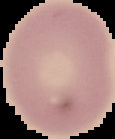

Summary:
  - Preparation: thin blood film
  - Image type: segmented cell region on a black background
  - Result: no malaria parasites seen
  - Image size: 115×139 pixels